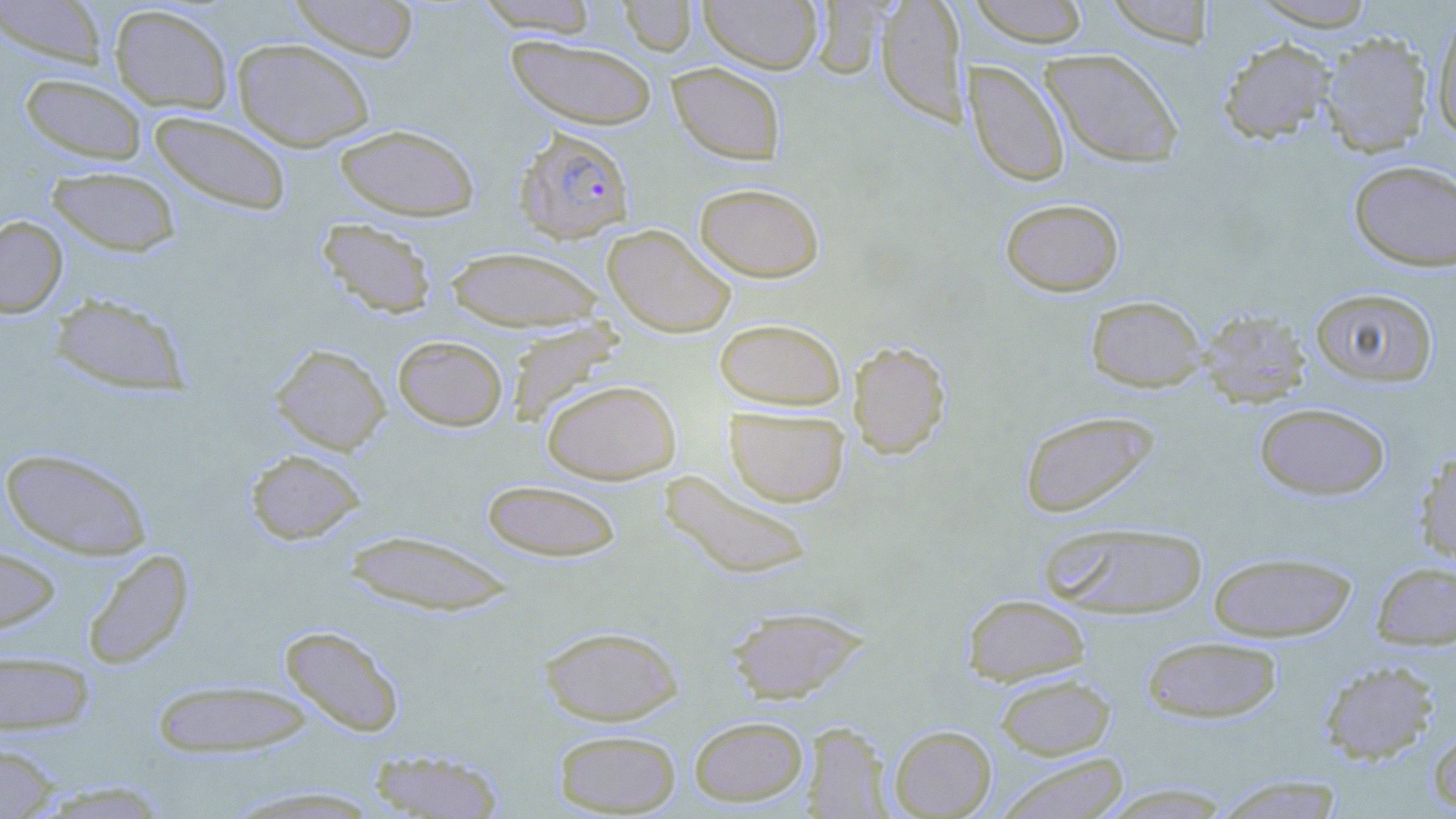
Summary:
  - Coordinate format: approximate bounding boxes as named x1/y1/x2/y2 corners in pixels
  - Uninfected red blood cell locations: (x1=0, y1=0, x2=109, y2=69), (x1=288, y1=0, x2=420, y2=62), (x1=473, y1=0, x2=601, y2=36), (x1=616, y1=0, x2=697, y2=56), (x1=698, y1=0, x2=823, y2=73), (x1=809, y1=0, x2=892, y2=80), (x1=875, y1=0, x2=970, y2=126), (x1=967, y1=0, x2=1092, y2=47), (x1=1103, y1=0, x2=1218, y2=47), (x1=1247, y1=1, x2=1378, y2=31), (x1=108, y1=4, x2=234, y2=113), (x1=1431, y1=10, x2=1456, y2=142), (x1=1319, y1=31, x2=1434, y2=158), (x1=507, y1=35, x2=658, y2=130), (x1=1217, y1=37, x2=1338, y2=144), (x1=232, y1=38, x2=375, y2=152), (x1=1040, y1=49, x2=1183, y2=168), (x1=964, y1=60, x2=1071, y2=188), (x1=667, y1=62, x2=787, y2=165), (x1=19, y1=73, x2=148, y2=165), (x1=149, y1=111, x2=292, y2=216), (x1=334, y1=123, x2=480, y2=221), (x1=1348, y1=159, x2=1456, y2=272), (x1=46, y1=165, x2=181, y2=257), (x1=694, y1=182, x2=825, y2=282), (x1=1000, y1=197, x2=1125, y2=296), (x1=0, y1=216, x2=68, y2=317), (x1=316, y1=218, x2=438, y2=319), (x1=603, y1=224, x2=736, y2=338), (x1=444, y1=246, x2=608, y2=332), (x1=1310, y1=287, x2=1439, y2=388), (x1=47, y1=292, x2=192, y2=395), (x1=1085, y1=295, x2=1208, y2=393), (x1=1198, y1=308, x2=1312, y2=408), (x1=714, y1=318, x2=846, y2=411), (x1=504, y1=320, x2=624, y2=427), (x1=392, y1=335, x2=509, y2=431), (x1=848, y1=340, x2=951, y2=459), (x1=270, y1=343, x2=391, y2=454), (x1=541, y1=379, x2=681, y2=484), (x1=1254, y1=402, x2=1391, y2=501), (x1=724, y1=406, x2=850, y2=507), (x1=1018, y1=410, x2=1161, y2=519), (x1=0, y1=447, x2=153, y2=560), (x1=1414, y1=448, x2=1456, y2=570), (x1=244, y1=449, x2=366, y2=545), (x1=660, y1=471, x2=814, y2=580), (x1=480, y1=479, x2=624, y2=562), (x1=1038, y1=521, x2=1210, y2=618), (x1=341, y1=530, x2=516, y2=616), (x1=0, y1=544, x2=62, y2=638), (x1=81, y1=549, x2=194, y2=670), (x1=1207, y1=551, x2=1358, y2=642), (x1=1370, y1=560, x2=1456, y2=650), (x1=961, y1=594, x2=1091, y2=686), (x1=725, y1=605, x2=868, y2=704), (x1=278, y1=624, x2=405, y2=738), (x1=538, y1=625, x2=684, y2=725), (x1=1142, y1=635, x2=1283, y2=723), (x1=0, y1=650, x2=96, y2=736), (x1=1318, y1=659, x2=1440, y2=764), (x1=995, y1=673, x2=1116, y2=760), (x1=151, y1=679, x2=314, y2=758), (x1=689, y1=715, x2=809, y2=806), (x1=1428, y1=717, x2=1456, y2=814), (x1=802, y1=722, x2=892, y2=817), (x1=889, y1=725, x2=997, y2=818), (x1=554, y1=729, x2=681, y2=816), (x1=0, y1=740, x2=62, y2=818), (x1=366, y1=748, x2=506, y2=819), (x1=996, y1=752, x2=1129, y2=819), (x1=1212, y1=775, x2=1347, y2=818), (x1=33, y1=780, x2=171, y2=818), (x1=224, y1=785, x2=386, y2=817)
  - Plasmodium falciparum-infected red blood cell locations: (x1=513, y1=127, x2=634, y2=244)
  - Slide-level diagnosis: Plasmodium falciparum
  - Stain: May-Grünwald-Giemsa
  - Field of view: single
  - Modality: optical microscopy
  - Image size: 1456×819 pixels
  - Magnification: 1000x
  - Preparation: thin blood film